Report the malaria status of this cell.
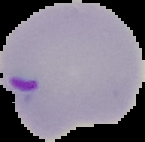

Parasitized.

Summary:
  - Image size: 145×142 pixels
  - Image type: segmented cell region on a black background
  - Preparation: thin blood film